Outline each Plasmodium ovale-infected red blood cell.
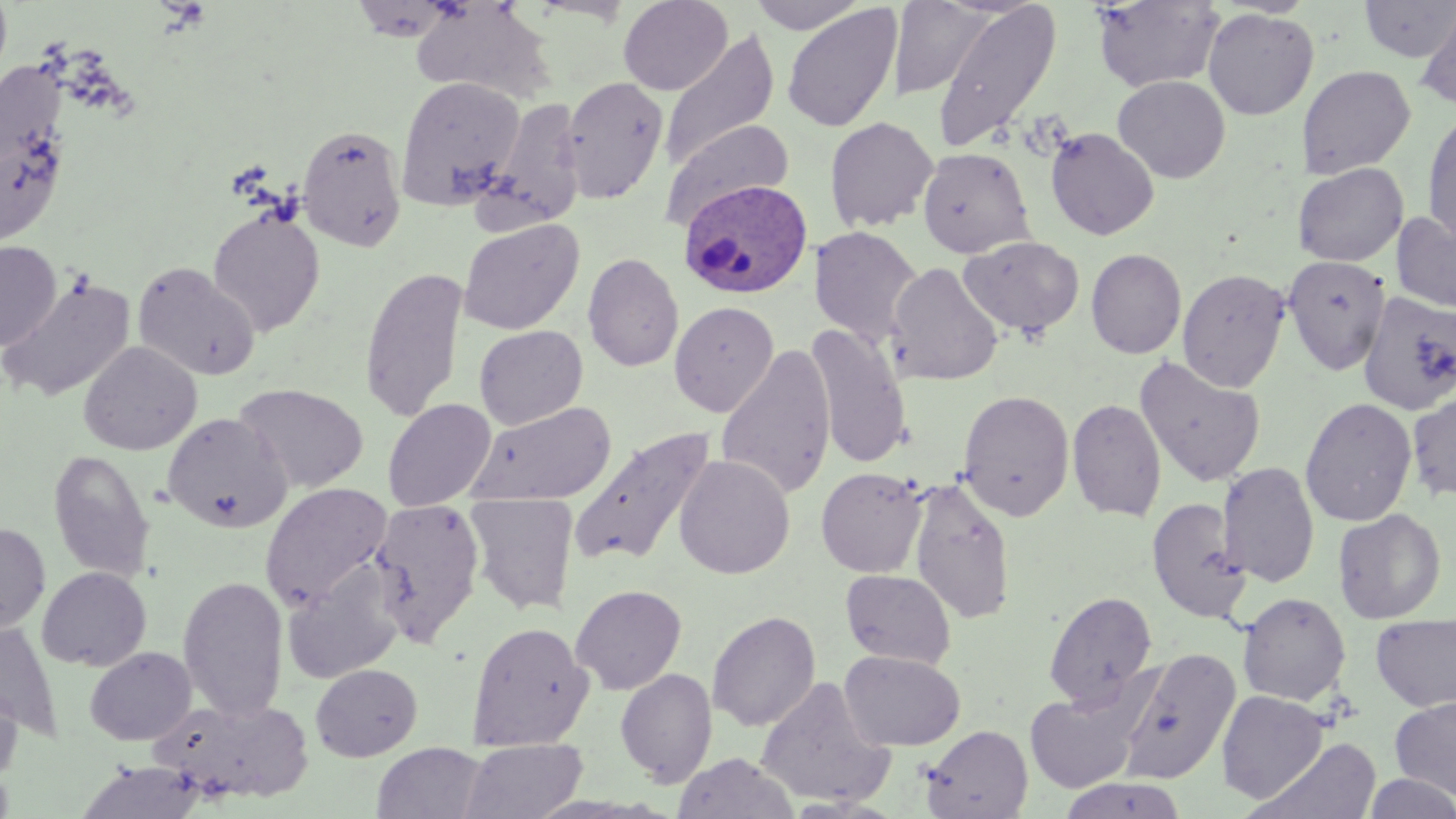

Approximate bounding boxes as named x1/y1/x2/y2 corners in pixels.
Plasmodium ovale-infected red blood cells: (x1=679, y1=178, x2=813, y2=300).

Summary:
  - Uninfected red blood cell locations: (x1=618, y1=0, x2=733, y2=95), (x1=748, y1=0, x2=869, y2=34), (x1=931, y1=0, x2=1061, y2=154), (x1=1359, y1=0, x2=1456, y2=62), (x1=410, y1=1, x2=556, y2=104), (x1=889, y1=1, x2=991, y2=99), (x1=1092, y1=1, x2=1224, y2=92), (x1=782, y1=4, x2=902, y2=133), (x1=1416, y1=5, x2=1456, y2=112), (x1=1202, y1=8, x2=1319, y2=121), (x1=659, y1=31, x2=779, y2=172), (x1=1297, y1=65, x2=1416, y2=179), (x1=395, y1=75, x2=524, y2=208), (x1=1112, y1=75, x2=1231, y2=183), (x1=560, y1=76, x2=669, y2=205), (x1=484, y1=99, x2=585, y2=230), (x1=1422, y1=110, x2=1456, y2=248), (x1=824, y1=116, x2=939, y2=233), (x1=664, y1=120, x2=794, y2=228), (x1=0, y1=122, x2=67, y2=250), (x1=296, y1=123, x2=408, y2=251), (x1=1045, y1=127, x2=1159, y2=240), (x1=917, y1=147, x2=1035, y2=258), (x1=1294, y1=162, x2=1409, y2=267), (x1=207, y1=207, x2=325, y2=337), (x1=1391, y1=210, x2=1456, y2=314), (x1=457, y1=218, x2=584, y2=335), (x1=811, y1=226, x2=923, y2=349), (x1=958, y1=236, x2=1084, y2=338), (x1=0, y1=240, x2=61, y2=351), (x1=1086, y1=248, x2=1186, y2=359), (x1=583, y1=252, x2=684, y2=372), (x1=1282, y1=255, x2=1391, y2=374), (x1=132, y1=261, x2=260, y2=381), (x1=886, y1=261, x2=1003, y2=386), (x1=360, y1=265, x2=469, y2=422), (x1=1178, y1=268, x2=1289, y2=392), (x1=0, y1=274, x2=136, y2=402), (x1=1358, y1=290, x2=1456, y2=415), (x1=669, y1=300, x2=779, y2=417), (x1=804, y1=322, x2=912, y2=470), (x1=474, y1=325, x2=588, y2=430), (x1=78, y1=341, x2=202, y2=455), (x1=716, y1=343, x2=836, y2=502), (x1=1133, y1=355, x2=1267, y2=488), (x1=235, y1=382, x2=369, y2=493), (x1=957, y1=388, x2=1075, y2=521), (x1=1406, y1=390, x2=1456, y2=502), (x1=1300, y1=397, x2=1417, y2=527), (x1=382, y1=398, x2=496, y2=511), (x1=1067, y1=398, x2=1167, y2=522), (x1=466, y1=401, x2=617, y2=507), (x1=162, y1=412, x2=292, y2=532), (x1=565, y1=424, x2=718, y2=570), (x1=48, y1=450, x2=154, y2=582), (x1=674, y1=454, x2=795, y2=579), (x1=1217, y1=460, x2=1319, y2=587), (x1=816, y1=467, x2=927, y2=578), (x1=907, y1=476, x2=1016, y2=625), (x1=261, y1=482, x2=392, y2=608), (x1=464, y1=493, x2=579, y2=616), (x1=1147, y1=497, x2=1250, y2=623), (x1=368, y1=498, x2=485, y2=646), (x1=1333, y1=508, x2=1446, y2=624), (x1=0, y1=522, x2=50, y2=633), (x1=283, y1=564, x2=405, y2=684), (x1=37, y1=566, x2=152, y2=671), (x1=840, y1=569, x2=956, y2=669), (x1=178, y1=575, x2=288, y2=722), (x1=571, y1=584, x2=687, y2=694), (x1=1044, y1=590, x2=1157, y2=709), (x1=1237, y1=592, x2=1351, y2=706), (x1=707, y1=610, x2=820, y2=733), (x1=1370, y1=612, x2=1456, y2=713), (x1=0, y1=620, x2=62, y2=740), (x1=467, y1=621, x2=594, y2=750), (x1=84, y1=646, x2=196, y2=746), (x1=1118, y1=647, x2=1241, y2=784), (x1=840, y1=650, x2=965, y2=750), (x1=310, y1=663, x2=422, y2=761), (x1=616, y1=668, x2=717, y2=787), (x1=755, y1=675, x2=896, y2=809), (x1=0, y1=680, x2=23, y2=783), (x1=1024, y1=685, x2=1149, y2=793), (x1=1216, y1=690, x2=1328, y2=803), (x1=151, y1=695, x2=315, y2=803), (x1=1389, y1=696, x2=1456, y2=800), (x1=919, y1=724, x2=1033, y2=819), (x1=1250, y1=737, x2=1381, y2=818), (x1=460, y1=738, x2=587, y2=819), (x1=373, y1=743, x2=488, y2=819), (x1=673, y1=752, x2=800, y2=819), (x1=75, y1=760, x2=207, y2=819), (x1=1363, y1=772, x2=1456, y2=818), (x1=1057, y1=777, x2=1189, y2=819)
  - Slide-level diagnosis: Plasmodium ovale
  - Preparation: thin blood smear
  - Magnification: 1000x
  - Modality: optical microscopy
  - Stain: May-Grünwald-Giemsa
  - Image size: 1456×819 pixels
  - Field of view: single